Point out each malaria parasite.
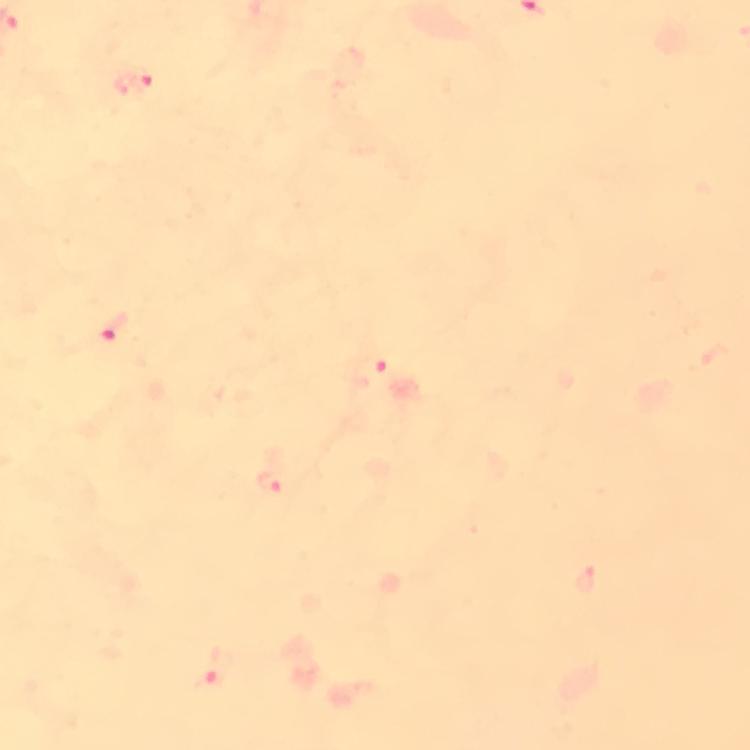

Approximate object centers, in pixels from the top-left corner.
Malaria parasites: (x=133, y=82), (x=117, y=330), (x=369, y=370), (x=273, y=483), (x=589, y=583), (x=214, y=673).

Immersion oil applied. Cropped region of a single field of view. Thick smear. Photographed with a smartphone mounted on the microscope. Image is 750×750 pixels. Giemsa stain. 100x magnification. From a malaria diagnostic workup.